Locate and identify every blood parasite.
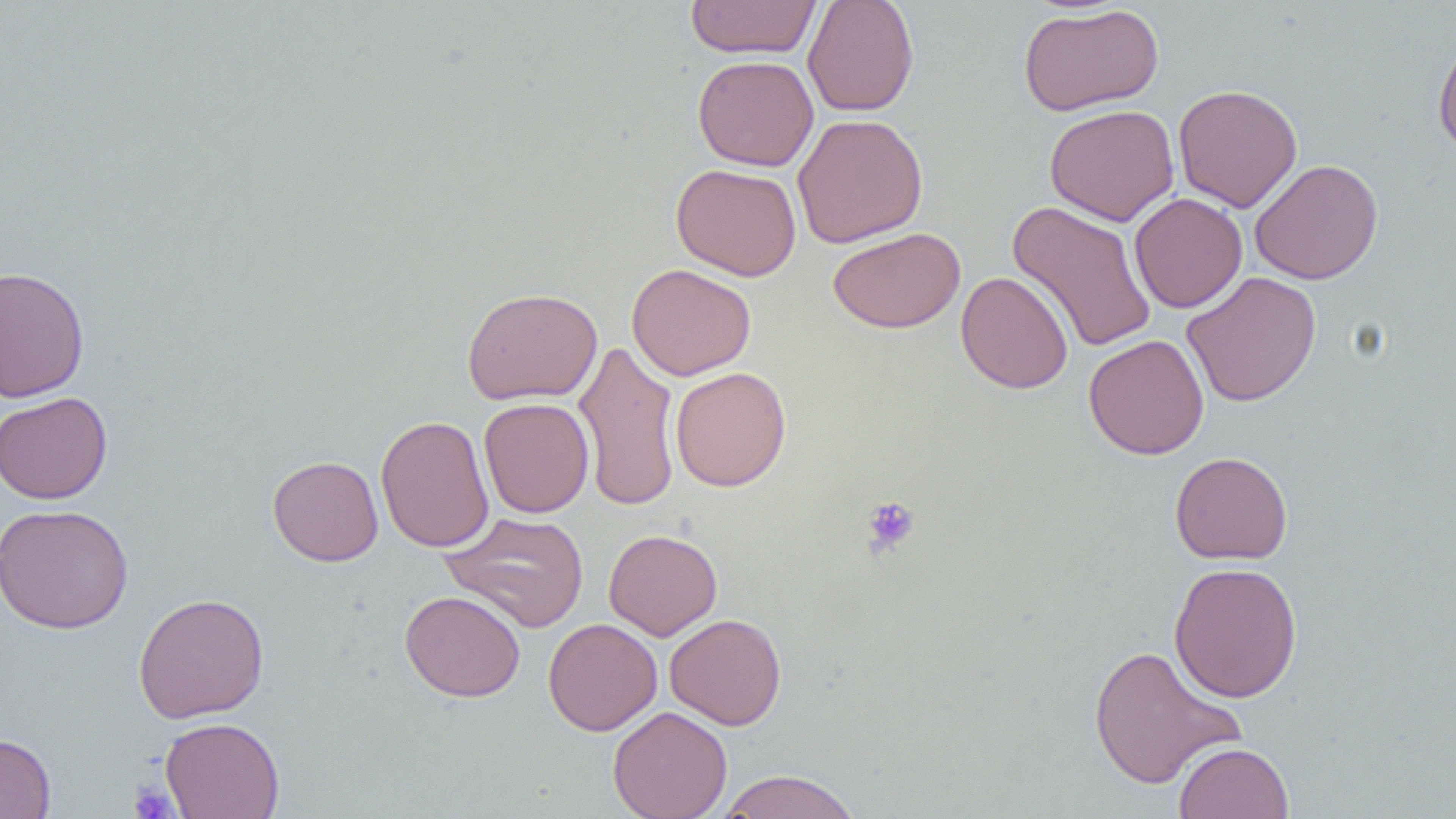

No blood parasites seen.

Summary:
  - Coordinate format: approximate bounding boxes as (x1, y1, x2, y2) in pixels
  - Platelet locations: (861, 496, 920, 556), (128, 782, 178, 818)
  - Uninfected red blood cell locations: (684, 0, 822, 60), (802, 0, 919, 117), (1018, 4, 1164, 116), (1432, 35, 1456, 160), (692, 54, 819, 171), (1173, 83, 1303, 213), (1045, 104, 1180, 227), (791, 113, 929, 248), (1249, 158, 1384, 285), (670, 162, 802, 281), (1129, 193, 1247, 313), (1007, 201, 1158, 354), (828, 227, 966, 333), (626, 263, 756, 381), (0, 265, 90, 403), (1181, 270, 1322, 408), (956, 271, 1074, 394), (461, 287, 602, 406), (1083, 333, 1209, 460), (573, 339, 681, 513), (670, 366, 791, 491), (0, 391, 113, 504), (479, 397, 594, 518), (375, 415, 494, 553), (1169, 451, 1293, 565), (268, 455, 383, 566), (0, 503, 134, 634), (440, 511, 589, 632), (603, 528, 722, 640), (1168, 561, 1303, 703), (400, 590, 525, 702), (133, 592, 270, 724), (664, 613, 787, 730), (542, 618, 662, 736), (1087, 643, 1246, 789), (607, 706, 732, 819), (160, 716, 285, 819), (0, 732, 56, 819), (1173, 741, 1293, 819), (714, 769, 862, 818)
  - Slide-level diagnosis: negative for blood parasites
  - Magnification: 1000x
  - Modality: optical microscopy
  - Preparation: thin blood film
  - Field of view: single
  - Image size: 1456×819 pixels